Comment on the morphology of the red blood cells.
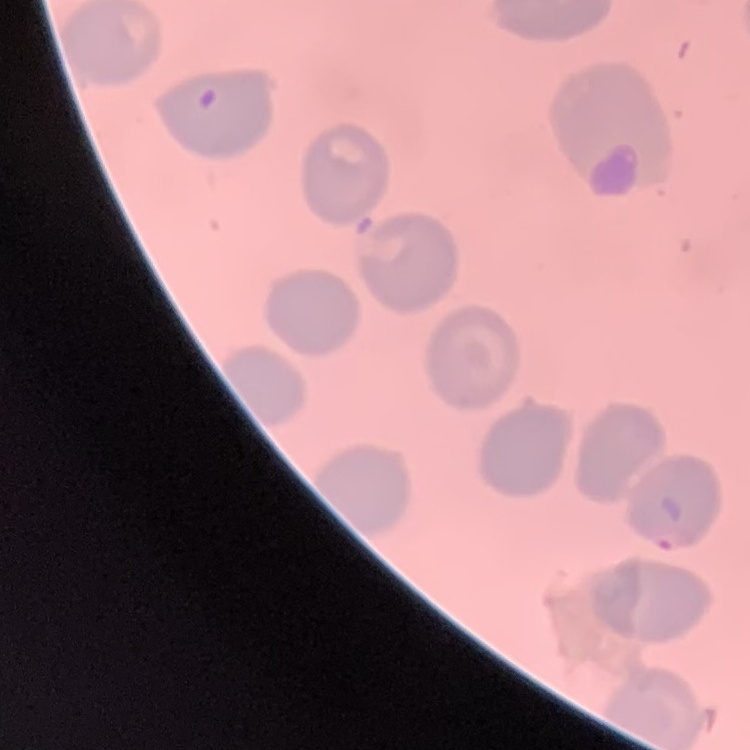

No rouleaux formation.

Summary:
  - Preparation: thin blood film
  - Image type: one tile cut from a larger photomicrograph
  - Stain: Field's or Giemsa